Report the malaria status of this cell.
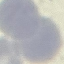

It is uninfected.

Cell patch, automatically extracted from a larger field of view and resized to 64 × 64 pixels. Giemsa-stained preparation. Thin blood smear. Acquired by smartphone through the microscope eyepiece.